Report the malaria status.
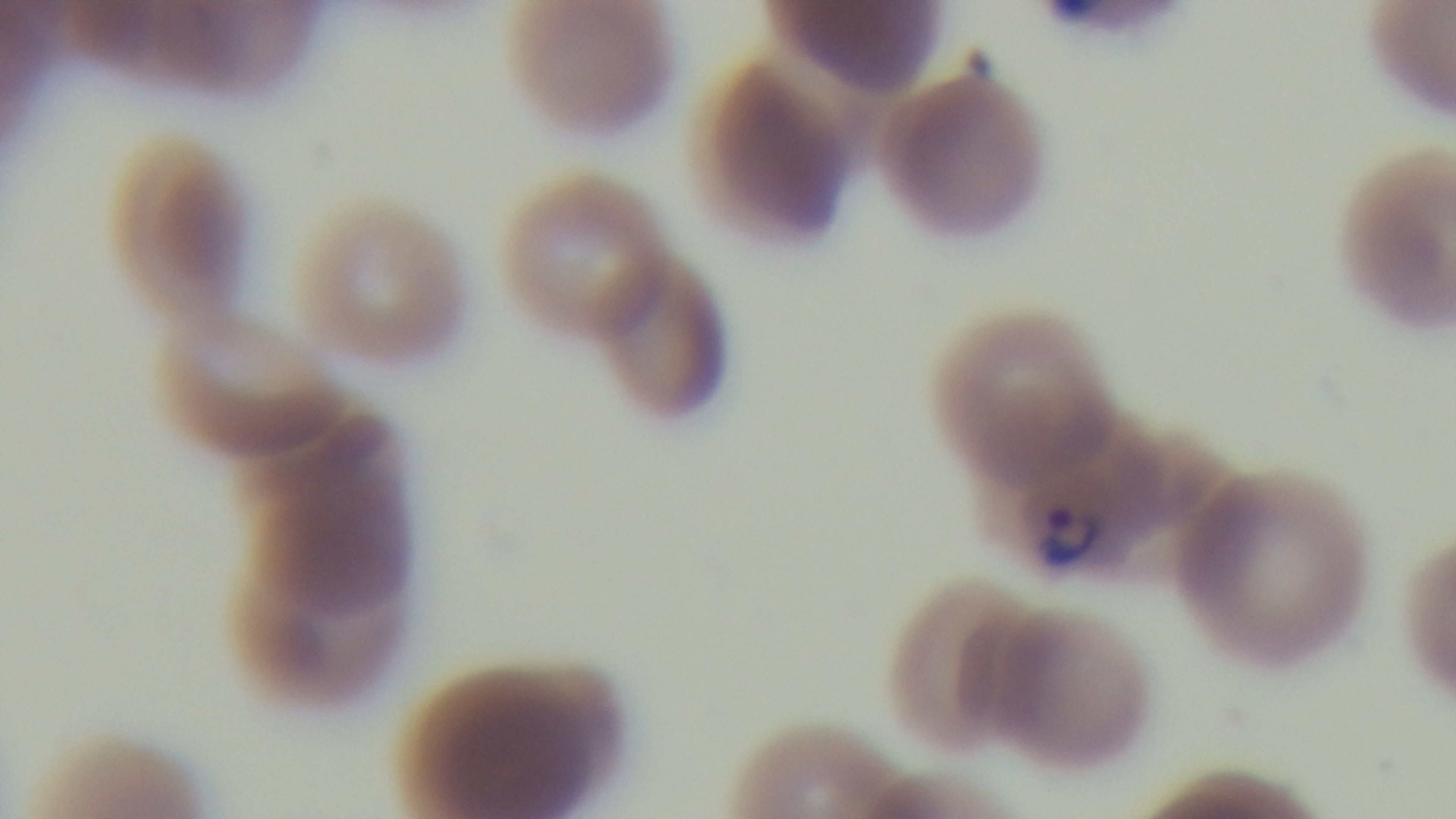
Infected.

preparation = thin smear
modality = light microscopy
objective = 100x oil immersion
stain = Giemsa
field of view = one from the slide
capture = mounted 4K digital camera